Assess this cell for malaria.
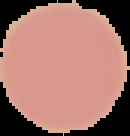
It is uninfected.

preparation = thin blood film
image size = 130×136 pixels
image type = segmented cell region with the area outside set to black